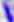
modality = micrograph
magnification = 400x
identification = Toxoplasma gondii